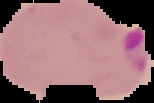

preparation = thin blood film
result = malaria parasites detected
image size = 154×103 pixels
image type = segmented cell region on a black background